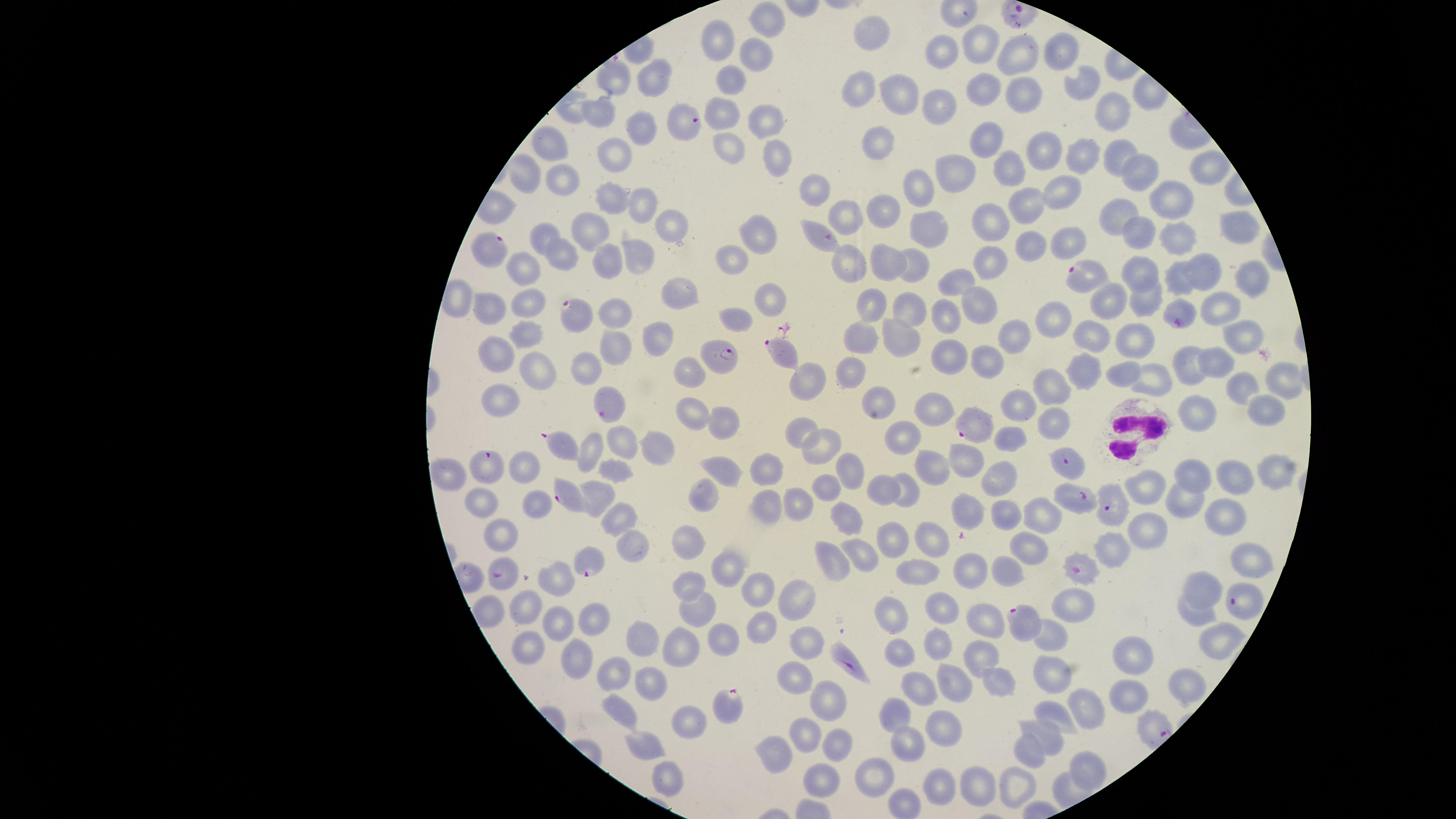

capture: smartphone photograph through the microscope eyepiece
visible_region: circular
image_size: 1456×819 pixels
parasitized_red_blood_cells: 'approximate marker points as [x, y] in pixels: [684, 128], [823, 236], [489, 247], [1082, 275], [577, 314], [1179, 316], [780, 349], [721, 354], [612, 403], [973, 424], [560, 443], [1067, 459], [483, 464], [567, 496], [1076, 496], [1114, 507], [590, 563], [1083, 570], [501, 575], [1244, 604], [1028, 622], [851, 662], [725, 709]'
preparation: thin blood smear
species: Plasmodium falciparum
stain: Giemsa
uninfected_red_blood_cells: 'approximate marker points as [x, y] in pixels: [767, 22], [871, 34], [716, 39], [980, 40], [940, 51], [1057, 51], [752, 54], [1018, 57], [612, 75], [652, 80], [732, 80], [1084, 84], [860, 88], [983, 90], [896, 91], [1027, 91], [934, 110], [721, 111], [595, 113], [1112, 113], [762, 122], [636, 129], [988, 139], [875, 144], [729, 146], [550, 148], [1118, 151], [1041, 152], [777, 156], [1084, 156], [615, 158], [1013, 163], [1203, 166], [957, 172], [526, 176], [1138, 176], [564, 182], [810, 185], [919, 188], [1062, 189], [611, 196], [1174, 197], [644, 204], [1025, 204], [882, 208], [1118, 212], [851, 213], [990, 223], [673, 225], [592, 226], [932, 226], [1239, 228], [543, 231], [1140, 231], [756, 234], [1074, 239], [1178, 239], [1030, 243], [637, 256], [731, 256], [559, 257], [606, 261], [846, 261], [989, 261], [1206, 261], [883, 264], [918, 264], [521, 265], [1142, 271], [1250, 275], [1179, 277], [960, 281], [680, 293], [767, 295], [1142, 297], [529, 302], [872, 302], [1107, 302], [974, 305], [1224, 305], [492, 308], [911, 310], [615, 313], [941, 317], [1055, 317], [734, 319], [526, 331], [1091, 333], [862, 334], [657, 337], [1018, 338], [1133, 338], [903, 341], [1243, 343], [615, 349], [493, 350], [954, 354], [996, 356], [1189, 358], [1219, 360], [585, 366], [1123, 367], [535, 368], [1084, 368], [847, 371], [691, 374], [1154, 378], [1284, 380], [1239, 383], [803, 385], [1049, 386], [875, 396], [1267, 401], [494, 402], [1022, 403], [1195, 409], [934, 410], [695, 414], [1055, 418], [722, 419], [801, 426], [903, 434], [1011, 434], [614, 441], [658, 442], [817, 447], [587, 451], [963, 462], [760, 465], [929, 466], [1277, 468], [521, 469], [616, 470], [844, 470], [723, 471], [1196, 473], [1232, 476], [454, 479], [1003, 481], [883, 488], [1146, 488], [827, 490], [906, 491], [599, 492], [702, 492], [1183, 497], [796, 499], [765, 503], [535, 505], [485, 506], [965, 507], [1003, 514], [1041, 516], [615, 517], [843, 519], [1223, 519], [1141, 532], [501, 535], [891, 536], [689, 540], [927, 542], [626, 546], [1025, 547], [1110, 550], [863, 554], [830, 560], [1249, 560], [725, 568], [971, 570], [1003, 573], [914, 575], [555, 580], [687, 583], [1203, 586], [757, 590], [794, 598], [1072, 607], [491, 610], [527, 610], [941, 610], [699, 613], [1193, 613], [890, 614], [591, 616], [988, 618], [558, 621], [761, 623], [1049, 635], [1228, 635], [722, 639], [805, 639], [643, 640], [678, 640], [528, 646], [936, 646], [979, 652], [577, 656], [896, 656], [1139, 656], [796, 675], [615, 677], [952, 679], [996, 679], [1053, 679], [649, 683], [1187, 689], [914, 690], [1129, 696], [827, 702], [1087, 710], [620, 712], [895, 714], [1056, 717], [683, 718], [944, 728], [804, 730], [1046, 739], [644, 747], [830, 748], [1026, 748], [910, 750], [775, 752], [1087, 762], [866, 773], [667, 775], [824, 779], [939, 781], [979, 785], [1018, 787], [904, 801]'
field_of_view: single
white_blood_cells: 'approximate marker points as [x, y] in pixels: [1129, 432]'
presence: malaria parasites detected